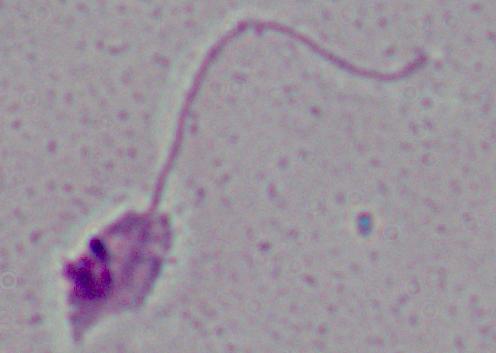
Summary:
  - Magnification: 1000x
  - Modality: photomicrograph
  - Identification: Leishmania